Locate every blood parasite and identify its species.
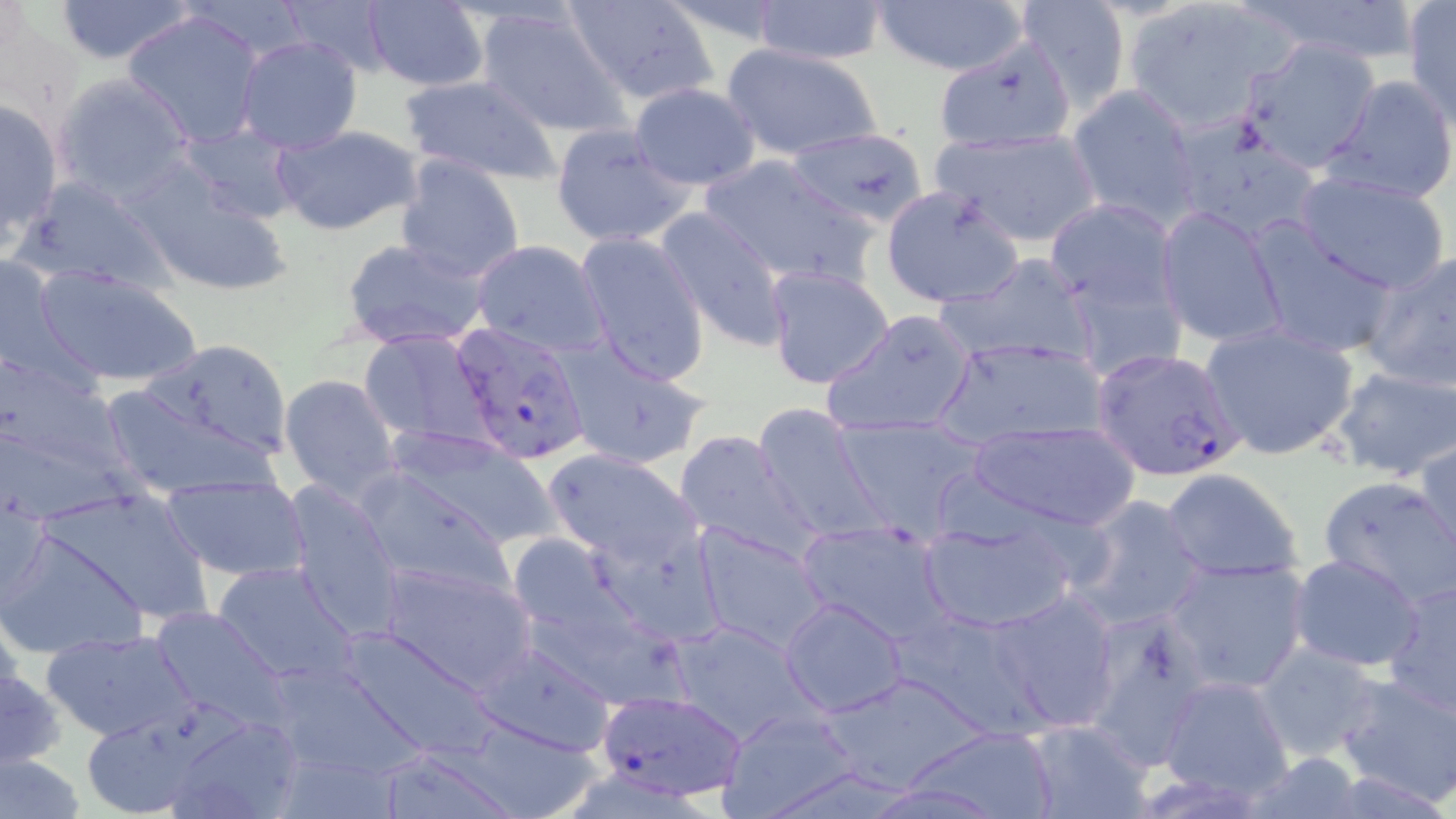

Approximate bounding boxes as named x1/y1/x2/y2 corners in pixels.
Plasmodium falciparum-infected red blood cells: (x1=454, y1=320, x2=591, y2=461), (x1=1090, y1=346, x2=1244, y2=480), (x1=596, y1=691, x2=745, y2=802).
No Plasmodium ovale, Plasmodium malariae, Plasmodium vivax, Babesia divergens, or Trypanosoma brucei observed.

Uninfected red blood cell locations: (x1=53, y1=0, x2=197, y2=64), (x1=282, y1=0, x2=394, y2=77), (x1=563, y1=0, x2=720, y2=106), (x1=869, y1=0, x2=1035, y2=75), (x1=1120, y1=0, x2=1293, y2=132), (x1=359, y1=1, x2=489, y2=90), (x1=749, y1=1, x2=889, y2=67), (x1=1012, y1=1, x2=1132, y2=110), (x1=1403, y1=3, x2=1456, y2=125), (x1=475, y1=4, x2=627, y2=138), (x1=122, y1=9, x2=267, y2=148), (x1=235, y1=35, x2=364, y2=155), (x1=1238, y1=36, x2=1381, y2=173), (x1=934, y1=37, x2=1078, y2=154), (x1=720, y1=44, x2=884, y2=161), (x1=54, y1=73, x2=195, y2=204), (x1=397, y1=74, x2=562, y2=185), (x1=1323, y1=74, x2=1456, y2=205), (x1=628, y1=83, x2=761, y2=192), (x1=1063, y1=85, x2=1204, y2=227), (x1=0, y1=96, x2=63, y2=246), (x1=1170, y1=117, x2=1324, y2=246), (x1=549, y1=121, x2=694, y2=249), (x1=176, y1=123, x2=302, y2=227), (x1=273, y1=125, x2=421, y2=236), (x1=926, y1=125, x2=1104, y2=247), (x1=787, y1=129, x2=930, y2=226), (x1=393, y1=154, x2=527, y2=283), (x1=698, y1=154, x2=874, y2=288), (x1=132, y1=169, x2=295, y2=298), (x1=1294, y1=170, x2=1452, y2=293), (x1=13, y1=175, x2=175, y2=297), (x1=880, y1=187, x2=1023, y2=309), (x1=1046, y1=198, x2=1181, y2=317), (x1=654, y1=206, x2=794, y2=352), (x1=1156, y1=206, x2=1287, y2=350), (x1=1245, y1=221, x2=1401, y2=360), (x1=574, y1=232, x2=712, y2=385), (x1=340, y1=237, x2=492, y2=352), (x1=470, y1=239, x2=608, y2=356), (x1=1359, y1=246, x2=1456, y2=394), (x1=1, y1=250, x2=76, y2=382), (x1=937, y1=254, x2=1100, y2=367), (x1=1061, y1=262, x2=1187, y2=383), (x1=33, y1=265, x2=202, y2=386), (x1=763, y1=265, x2=896, y2=390), (x1=823, y1=309, x2=981, y2=439), (x1=1199, y1=322, x2=1360, y2=461), (x1=359, y1=329, x2=494, y2=449), (x1=933, y1=336, x2=1112, y2=446), (x1=553, y1=337, x2=714, y2=471), (x1=137, y1=338, x2=295, y2=461), (x1=0, y1=357, x2=130, y2=486), (x1=1330, y1=364, x2=1456, y2=480), (x1=279, y1=372, x2=403, y2=501), (x1=103, y1=384, x2=276, y2=497), (x1=753, y1=402, x2=887, y2=546), (x1=831, y1=414, x2=990, y2=541), (x1=969, y1=420, x2=1135, y2=532), (x1=387, y1=426, x2=560, y2=553), (x1=673, y1=429, x2=819, y2=562), (x1=1416, y1=438, x2=1456, y2=563), (x1=543, y1=448, x2=700, y2=568), (x1=355, y1=469, x2=514, y2=596), (x1=1161, y1=469, x2=1304, y2=581), (x1=161, y1=475, x2=312, y2=582), (x1=1318, y1=475, x2=1454, y2=609), (x1=278, y1=480, x2=406, y2=638), (x1=36, y1=485, x2=216, y2=627), (x1=1, y1=489, x2=50, y2=611), (x1=1071, y1=494, x2=1209, y2=632), (x1=917, y1=513, x2=1082, y2=633), (x1=796, y1=518, x2=957, y2=648), (x1=589, y1=520, x2=724, y2=646), (x1=691, y1=524, x2=831, y2=655), (x1=2, y1=529, x2=145, y2=660), (x1=1287, y1=553, x2=1425, y2=673), (x1=1161, y1=556, x2=1310, y2=692), (x1=210, y1=559, x2=361, y2=687), (x1=376, y1=560, x2=538, y2=695), (x1=1382, y1=576, x2=1456, y2=717), (x1=988, y1=591, x2=1122, y2=730), (x1=780, y1=598, x2=909, y2=717), (x1=150, y1=605, x2=291, y2=728), (x1=898, y1=609, x2=1049, y2=740), (x1=1076, y1=618, x2=1211, y2=776), (x1=665, y1=620, x2=817, y2=746), (x1=332, y1=626, x2=505, y2=762), (x1=43, y1=630, x2=198, y2=743), (x1=468, y1=636, x2=617, y2=756), (x1=1254, y1=641, x2=1383, y2=760), (x1=259, y1=656, x2=438, y2=788), (x1=0, y1=666, x2=66, y2=770), (x1=1333, y1=669, x2=1456, y2=807), (x1=1157, y1=676, x2=1295, y2=805), (x1=715, y1=707, x2=861, y2=818), (x1=167, y1=711, x2=305, y2=819), (x1=78, y1=713, x2=222, y2=818), (x1=1021, y1=721, x2=1152, y2=819), (x1=901, y1=726, x2=1056, y2=816), (x1=373, y1=746, x2=521, y2=818), (x1=0, y1=753, x2=86, y2=819). Slide-level diagnosis: Plasmodium falciparum. May-Grünwald-Giemsa-stained preparation. One field of a larger specimen. Captured at 1000x magnification. Image is 1456×819 pixels. Thin blood smear. Optical microscopy.